Comment on the morphology of the red blood cells.
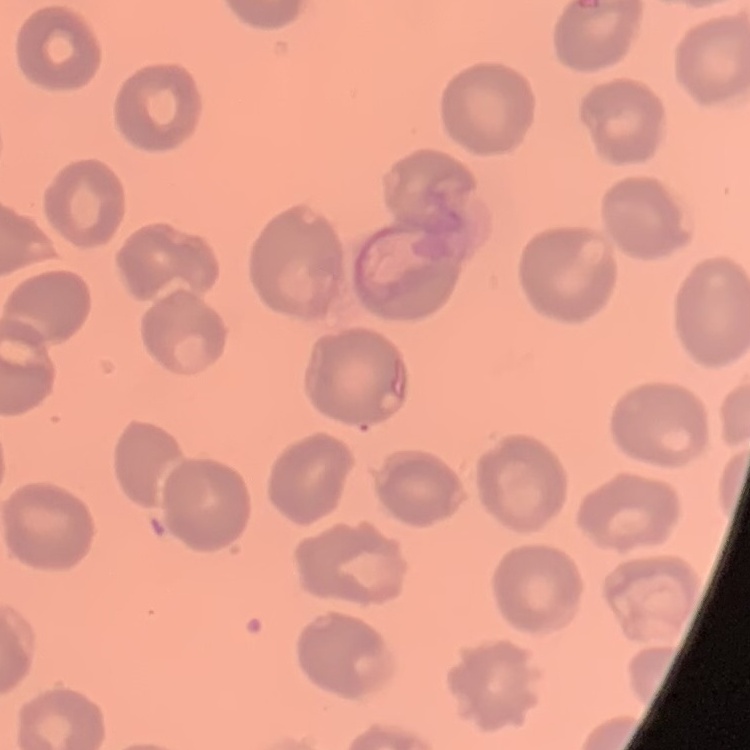
They show no rouleaux formation.

Thin peripheral smear. Stained with either Field's or Giemsa. Square crop of a larger photomicrograph.